Classify this cell by malaria status.
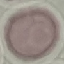
Uninfected.

Acquired by smartphone through the microscope eyepiece. Cell patch, automatically extracted from a larger field of view and resized to 64 × 64 pixels. Giemsa-stained preparation. Thin smear of blood.